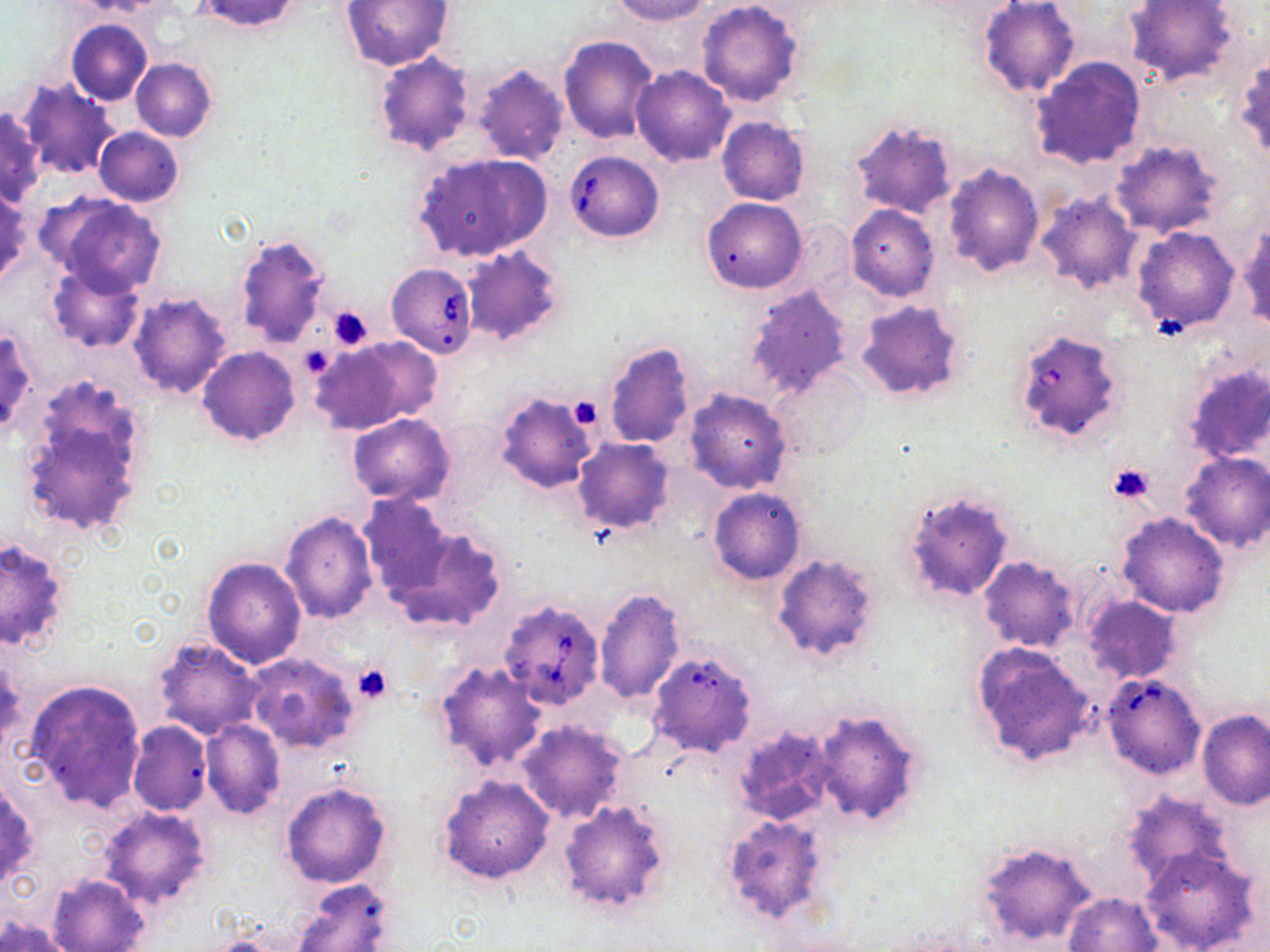

slide_level_diagnosis: Babesia divergens
platelet_locations: 'approximate bounding boxes as [x1, y1, x2, y2] in pixels: [328, 306, 375, 350], [304, 351, 333, 376], [566, 398, 602, 431], [1107, 462, 1157, 504], [351, 664, 392, 703]'
modality: light microscopy
field_of_view: one of a larger specimen
magnification: 1000x
babesia_divergens_infected_red_blood_cell_locations: 'approximate bounding boxes as [x1, y1, x2, y2] in pixels: [565, 150, 664, 243], [385, 264, 478, 359], [1011, 326, 1125, 445], [497, 599, 605, 709], [1101, 673, 1205, 780]'
preparation: thin blood film
uninfected_red_blood_cell_locations: 'approximate bounding boxes as [x1, y1, x2, y2] in pixels: [192, 0, 303, 33], [608, 0, 713, 24], [696, 0, 805, 107], [1125, 0, 1239, 88], [343, 1, 452, 72], [977, 2, 1080, 98], [66, 19, 153, 104], [1002, 26, 1126, 148], [558, 34, 658, 144], [373, 53, 474, 156], [1233, 55, 1270, 164], [131, 58, 217, 141], [1029, 58, 1147, 171], [470, 65, 569, 165], [631, 66, 735, 166], [18, 79, 121, 180], [0, 105, 45, 208], [717, 117, 810, 206], [848, 118, 957, 220], [93, 127, 184, 207], [1109, 140, 1224, 238], [413, 151, 552, 261], [942, 163, 1045, 276], [0, 189, 29, 290], [1034, 192, 1141, 295], [47, 195, 167, 297], [701, 197, 807, 293], [846, 204, 940, 301], [1238, 224, 1269, 329], [1130, 226, 1241, 334], [234, 234, 330, 349], [462, 244, 567, 347], [47, 263, 144, 353], [743, 284, 853, 400], [127, 293, 232, 398], [856, 299, 966, 404], [0, 324, 37, 441], [309, 335, 439, 437], [602, 342, 696, 450], [198, 345, 300, 445], [1180, 361, 1270, 466], [768, 365, 873, 464], [19, 381, 152, 544], [683, 389, 794, 493], [495, 392, 598, 493], [346, 412, 454, 505], [571, 437, 675, 534], [1178, 451, 1270, 554], [708, 487, 805, 585], [900, 488, 1016, 603], [358, 494, 458, 597], [280, 512, 377, 624], [1117, 513, 1228, 617], [379, 516, 507, 633], [0, 535, 71, 656], [771, 554, 884, 664], [201, 556, 306, 668], [978, 556, 1080, 652], [594, 585, 687, 705], [1080, 594, 1182, 684], [152, 637, 265, 740], [970, 641, 1098, 769], [1, 653, 22, 755], [244, 653, 358, 755], [435, 661, 547, 775], [25, 678, 145, 814], [808, 707, 926, 828], [1198, 710, 1269, 809], [199, 720, 285, 820], [517, 720, 629, 824], [127, 721, 211, 816], [730, 722, 834, 826], [437, 775, 555, 885], [0, 776, 38, 889], [280, 781, 391, 889], [1118, 788, 1237, 893], [557, 797, 673, 916], [97, 806, 212, 912], [720, 814, 833, 928], [973, 839, 1099, 949], [1139, 847, 1263, 952], [47, 874, 150, 952], [291, 879, 396, 952], [1064, 892, 1163, 952], [1, 914, 76, 951]'
stain: May-Grünwald-Giemsa
image_size: 1270×952 pixels